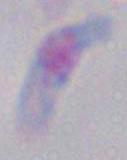
Summary:
  - Magnification: 1000x
  - Modality: photomicrograph
  - Identification: Toxoplasma gondii